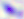
Toxoplasma gondii is seen. 400x magnification. Micrograph.